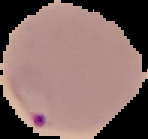
preparation = thin blood film
malaria status = parasitized
image type = segmented cell region on a black background
image size = 148×139 pixels